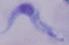

1000x magnification. Photomicrograph. A trypanosome is shown.